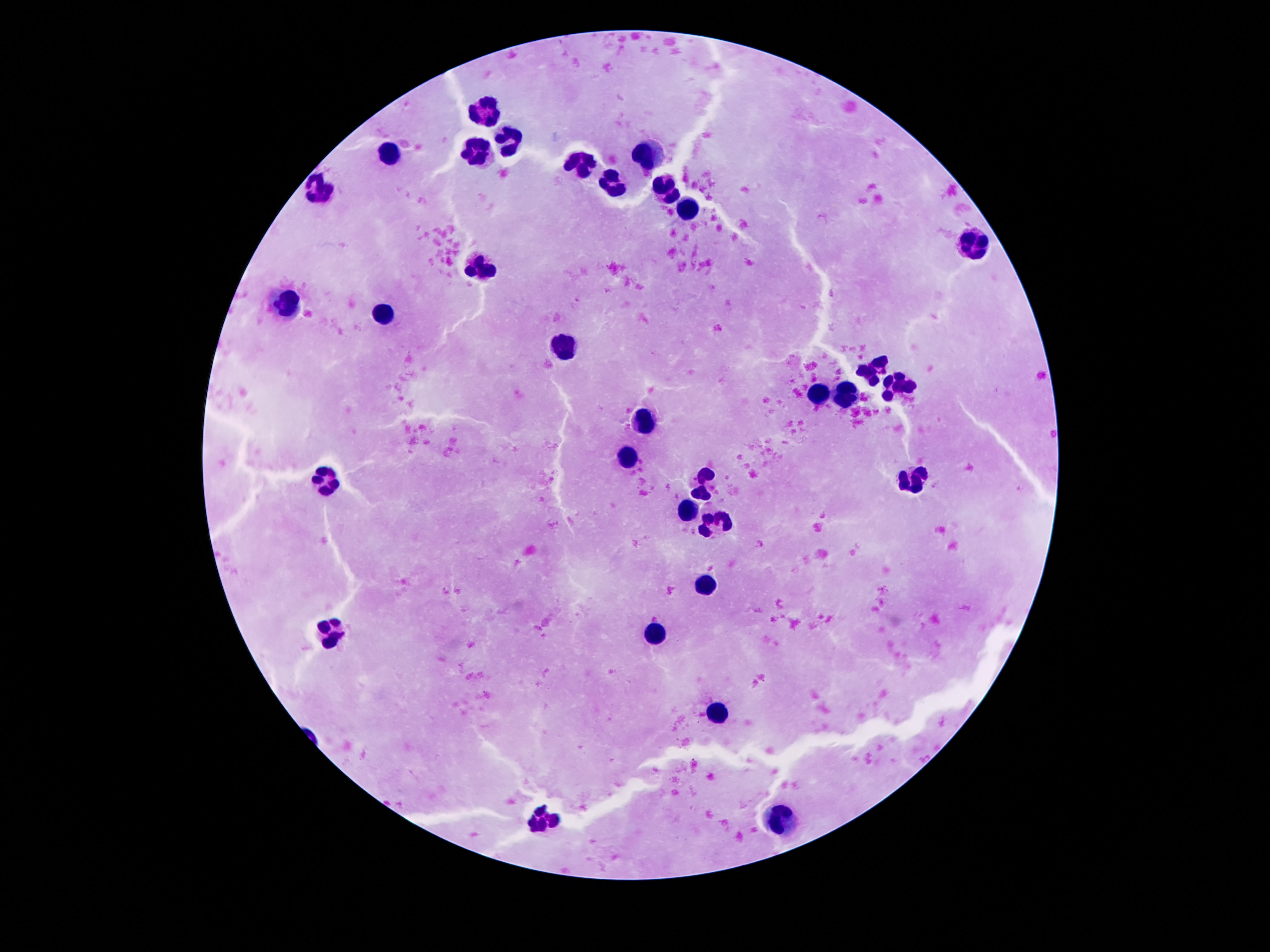

preparation = thick blood smear
stain = Giemsa
magnification = 100x
leukocyte locations = approximate centers as {x, y} in pixels: {487, 116}, {508, 139}, {646, 146}, {476, 151}, {390, 152}, {579, 164}, {611, 184}, {319, 186}, {663, 190}, {687, 208}, {975, 244}, {476, 259}, {284, 302}, {383, 313}, {558, 345}, {876, 368}, {895, 386}, {816, 395}, {844, 399}, {644, 419}, {629, 456}, {327, 477}, {704, 478}, {915, 478}, {689, 508}, {713, 520}, {708, 582}, {332, 631}, {652, 632}, {721, 711}, {545, 819}, {783, 820}
patient malaria status = not infected
capture = smartphone camera through the microscope eyepiece
field of view = single
image size = 1270×952 pixels